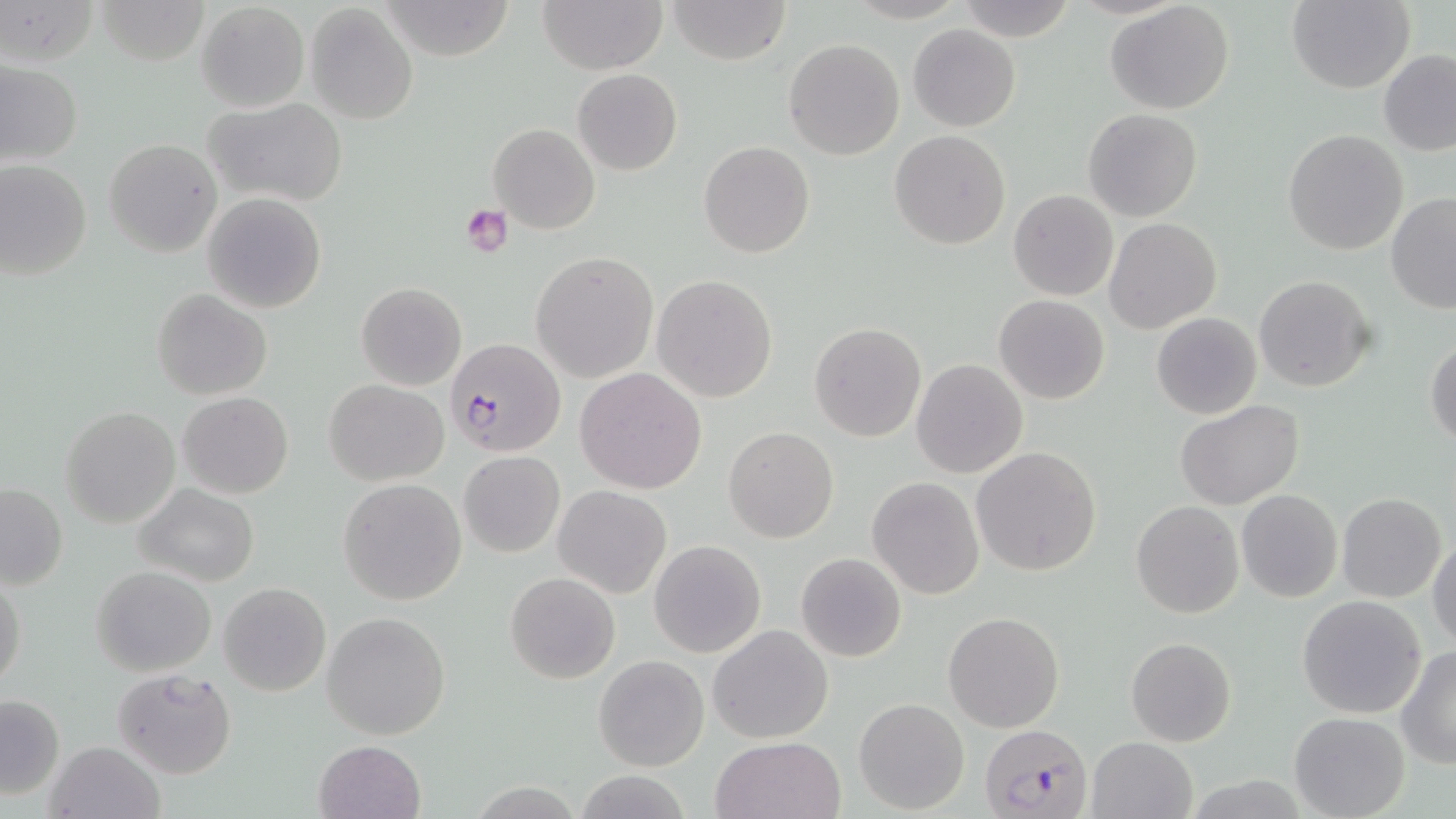
Summary:
  - Coordinate format: approximate bounding boxes as (x1, y1, x2, y2) in pixels
  - Plasmodium falciparum-infected red blood cell locations: (444, 339, 564, 456), (979, 722, 1090, 818)
  - Uninfected red blood cell locations: (2, 0, 100, 69), (94, 0, 212, 66), (378, 0, 515, 61), (538, 0, 668, 73), (667, 0, 792, 65), (954, 0, 1075, 39), (1287, 0, 1414, 93), (196, 2, 309, 113), (1106, 3, 1236, 115), (304, 4, 419, 125), (908, 25, 1020, 131), (783, 38, 905, 160), (1378, 49, 1456, 156), (1, 62, 82, 168), (572, 69, 683, 175), (204, 96, 349, 208), (1083, 108, 1202, 222), (488, 122, 600, 234), (889, 129, 1011, 250), (1282, 129, 1409, 255), (104, 137, 223, 257), (699, 140, 815, 258), (0, 160, 92, 280), (1008, 189, 1119, 301), (203, 192, 327, 312), (1386, 193, 1456, 312), (1103, 218, 1221, 335), (531, 252, 658, 383), (651, 274, 778, 403), (1253, 274, 1377, 392), (355, 281, 468, 390), (151, 289, 272, 399), (993, 294, 1110, 405), (1152, 312, 1261, 419), (809, 322, 925, 441), (1425, 337, 1456, 448), (911, 358, 1028, 478), (574, 367, 707, 494), (324, 379, 449, 485), (176, 392, 294, 498), (1176, 399, 1305, 510), (60, 406, 181, 529), (724, 426, 839, 543), (972, 446, 1103, 576), (458, 451, 565, 557), (867, 477, 985, 600), (339, 478, 467, 606), (0, 483, 68, 590), (135, 484, 260, 588), (553, 485, 672, 599), (1236, 490, 1343, 603), (1338, 493, 1448, 603), (1132, 501, 1244, 619), (1429, 532, 1455, 651), (649, 539, 766, 657), (796, 552, 906, 662), (91, 565, 215, 676), (505, 572, 620, 683), (0, 573, 27, 692), (218, 582, 332, 697), (1297, 595, 1427, 719), (322, 610, 452, 740), (943, 611, 1066, 732), (708, 624, 833, 745), (1125, 638, 1236, 748), (1397, 649, 1456, 768), (592, 655, 709, 771), (112, 667, 237, 778), (0, 692, 64, 801), (853, 697, 970, 815), (1289, 712, 1409, 819), (709, 735, 845, 819), (1086, 736, 1199, 819), (46, 740, 165, 819), (314, 740, 427, 819), (580, 774, 701, 819), (473, 784, 582, 819)
  - Platelet locations: (459, 204, 513, 257)
  - Slide-level diagnosis: Plasmodium falciparum
  - Magnification: 1000x
  - Image size: 1456×819 pixels
  - Modality: light microscopy
  - Stain: May-Grünwald-Giemsa
  - Field of view: single
  - Preparation: thin blood smear